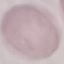

result = negative for malaria parasites
image type = cell patch, automatically extracted from a larger field of view and resized to 64 × 64 pixels
preparation = thin blood smear
stain = Giemsa
capture = smartphone camera at the microscope eyepiece